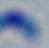 Toxoplasma gondii is shown. Photomicrograph. 1000x magnification.